Identify the blood parasite species.
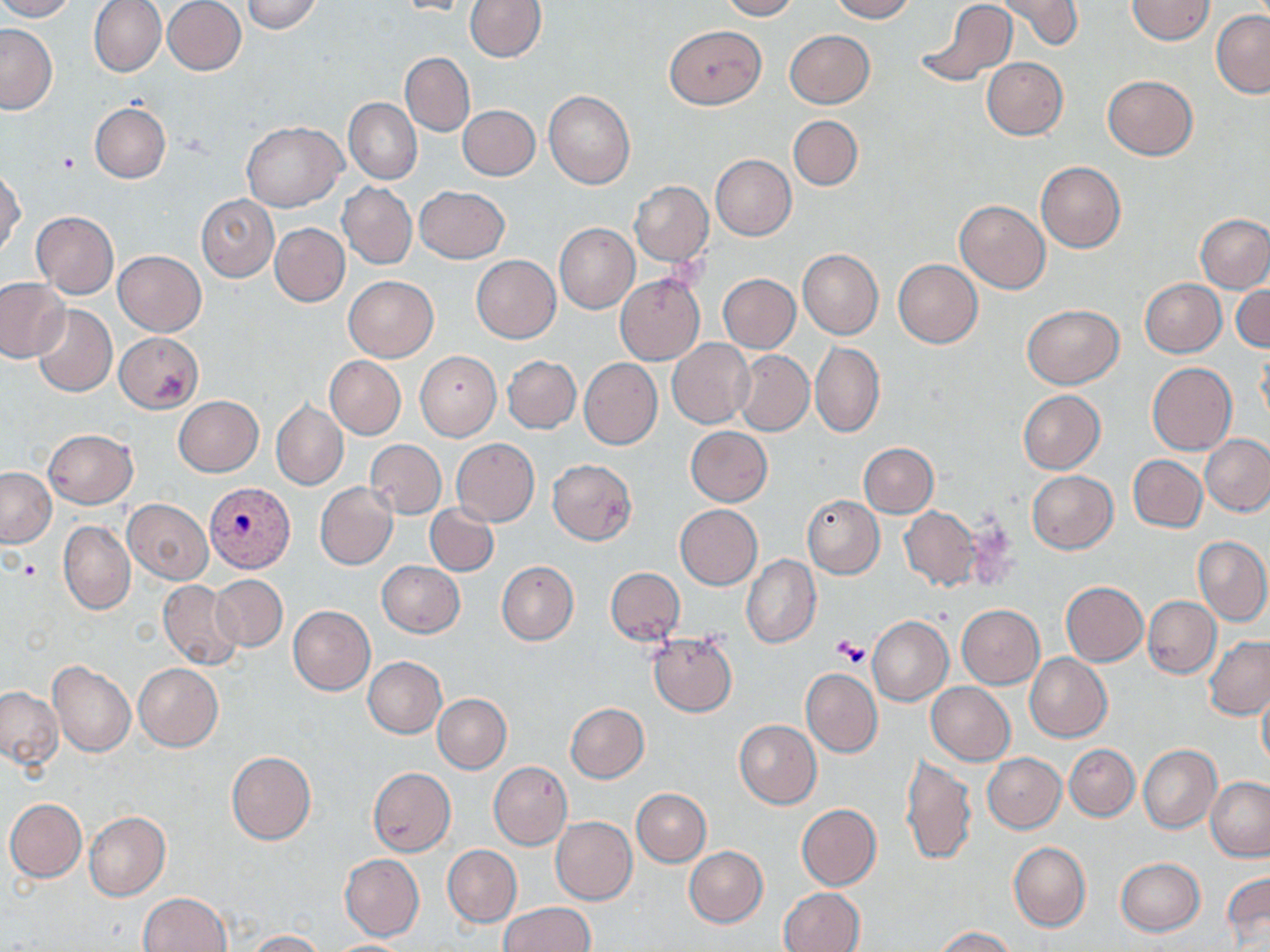

Plasmodium vivax.

Summary:
  - Coordinate format: approximate bounding boxes as named x1/y1/x2/y2 corners in pixels
  - Platelet locations: (x1=57, y1=151, x2=79, y2=172), (x1=832, y1=637, x2=869, y2=667)
  - Plasmodium vivax-infected red blood cell locations: (x1=203, y1=482, x2=294, y2=573)
  - Uninfected red blood cell locations: (x1=0, y1=0, x2=76, y2=22), (x1=89, y1=0, x2=166, y2=77), (x1=465, y1=0, x2=545, y2=62), (x1=719, y1=0, x2=798, y2=20), (x1=829, y1=0, x2=914, y2=21), (x1=918, y1=0, x2=1017, y2=88), (x1=996, y1=0, x2=1084, y2=51), (x1=1126, y1=0, x2=1215, y2=44), (x1=162, y1=1, x2=246, y2=75), (x1=240, y1=1, x2=325, y2=33), (x1=390, y1=1, x2=478, y2=16), (x1=1211, y1=10, x2=1270, y2=97), (x1=0, y1=23, x2=56, y2=114), (x1=665, y1=25, x2=765, y2=108), (x1=784, y1=30, x2=874, y2=109), (x1=401, y1=52, x2=475, y2=136), (x1=981, y1=58, x2=1068, y2=139), (x1=1102, y1=74, x2=1198, y2=160), (x1=544, y1=90, x2=636, y2=189), (x1=344, y1=99, x2=421, y2=183), (x1=90, y1=103, x2=170, y2=183), (x1=458, y1=105, x2=540, y2=181), (x1=788, y1=115, x2=863, y2=190), (x1=241, y1=120, x2=346, y2=211), (x1=710, y1=154, x2=796, y2=240), (x1=1036, y1=161, x2=1125, y2=252), (x1=1, y1=167, x2=24, y2=257), (x1=630, y1=181, x2=713, y2=265), (x1=339, y1=183, x2=416, y2=268), (x1=414, y1=185, x2=509, y2=262), (x1=196, y1=195, x2=278, y2=282), (x1=955, y1=200, x2=1051, y2=294), (x1=30, y1=211, x2=119, y2=298), (x1=1196, y1=214, x2=1270, y2=291), (x1=554, y1=222, x2=639, y2=314), (x1=270, y1=223, x2=349, y2=307), (x1=114, y1=250, x2=206, y2=336), (x1=798, y1=250, x2=883, y2=339), (x1=471, y1=255, x2=560, y2=343), (x1=894, y1=259, x2=982, y2=347), (x1=615, y1=273, x2=705, y2=364), (x1=718, y1=274, x2=799, y2=353), (x1=343, y1=276, x2=439, y2=363), (x1=0, y1=278, x2=70, y2=363), (x1=1139, y1=278, x2=1226, y2=356), (x1=1232, y1=283, x2=1270, y2=352), (x1=1022, y1=304, x2=1123, y2=387), (x1=32, y1=305, x2=117, y2=397), (x1=114, y1=332, x2=204, y2=413), (x1=668, y1=339, x2=755, y2=429), (x1=811, y1=341, x2=885, y2=438), (x1=1257, y1=348, x2=1270, y2=433), (x1=734, y1=350, x2=814, y2=436), (x1=415, y1=351, x2=501, y2=440), (x1=325, y1=355, x2=406, y2=439), (x1=503, y1=355, x2=581, y2=434), (x1=580, y1=358, x2=662, y2=449), (x1=1147, y1=363, x2=1237, y2=455), (x1=1018, y1=390, x2=1105, y2=474), (x1=173, y1=396, x2=263, y2=477), (x1=271, y1=401, x2=348, y2=491), (x1=685, y1=427, x2=773, y2=506), (x1=43, y1=429, x2=138, y2=508), (x1=1202, y1=434, x2=1270, y2=515), (x1=365, y1=439, x2=446, y2=518), (x1=452, y1=439, x2=539, y2=526), (x1=859, y1=442, x2=938, y2=517), (x1=1128, y1=455, x2=1207, y2=533), (x1=547, y1=459, x2=637, y2=545), (x1=0, y1=467, x2=55, y2=546), (x1=1027, y1=470, x2=1117, y2=553), (x1=315, y1=483, x2=398, y2=570), (x1=803, y1=496, x2=884, y2=578), (x1=123, y1=499, x2=213, y2=584), (x1=426, y1=503, x2=499, y2=575), (x1=675, y1=504, x2=762, y2=589), (x1=900, y1=506, x2=981, y2=591), (x1=53, y1=509, x2=211, y2=597), (x1=59, y1=521, x2=135, y2=614), (x1=1192, y1=535, x2=1270, y2=625), (x1=742, y1=555, x2=821, y2=649), (x1=496, y1=560, x2=578, y2=645), (x1=377, y1=561, x2=464, y2=637), (x1=606, y1=567, x2=684, y2=645), (x1=211, y1=574, x2=288, y2=652), (x1=158, y1=580, x2=244, y2=668), (x1=1060, y1=581, x2=1148, y2=666), (x1=1143, y1=596, x2=1220, y2=679), (x1=956, y1=604, x2=1045, y2=689), (x1=288, y1=605, x2=375, y2=695), (x1=867, y1=616, x2=952, y2=705), (x1=647, y1=632, x2=738, y2=716), (x1=1203, y1=635, x2=1270, y2=720), (x1=1025, y1=653, x2=1112, y2=741), (x1=363, y1=656, x2=447, y2=737), (x1=47, y1=661, x2=135, y2=757), (x1=134, y1=663, x2=223, y2=751), (x1=800, y1=668, x2=882, y2=756), (x1=1257, y1=681, x2=1270, y2=775), (x1=927, y1=682, x2=1016, y2=765), (x1=0, y1=687, x2=63, y2=768), (x1=433, y1=693, x2=511, y2=773), (x1=565, y1=702, x2=649, y2=782), (x1=735, y1=719, x2=821, y2=808), (x1=1065, y1=744, x2=1140, y2=821), (x1=1137, y1=745, x2=1221, y2=832), (x1=226, y1=751, x2=316, y2=844), (x1=983, y1=753, x2=1064, y2=832), (x1=901, y1=754, x2=976, y2=866), (x1=488, y1=761, x2=572, y2=850), (x1=367, y1=768, x2=455, y2=856), (x1=1206, y1=777, x2=1270, y2=861), (x1=632, y1=788, x2=710, y2=866), (x1=4, y1=798, x2=86, y2=882), (x1=797, y1=804, x2=880, y2=890), (x1=84, y1=811, x2=171, y2=900), (x1=551, y1=816, x2=637, y2=906), (x1=1009, y1=841, x2=1090, y2=931), (x1=442, y1=845, x2=521, y2=926), (x1=685, y1=846, x2=767, y2=927), (x1=339, y1=854, x2=424, y2=940), (x1=1115, y1=857, x2=1206, y2=936), (x1=1222, y1=870, x2=1269, y2=951), (x1=779, y1=888, x2=864, y2=952), (x1=139, y1=892, x2=232, y2=952), (x1=500, y1=902, x2=594, y2=952), (x1=933, y1=926, x2=1019, y2=952), (x1=248, y1=930, x2=328, y2=951), (x1=323, y1=939, x2=416, y2=951)
  - Modality: light microscopy
  - Magnification: 1000x
  - Stain: May-Grünwald-Giemsa
  - Preparation: thin blood smear
  - Image size: 1270×952 pixels
  - Field of view: single